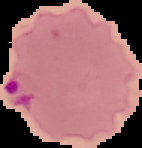
From a thin blood smear. Image is 142×148 pixels. Malaria status: parasitized. Segmented cell region on a black background.